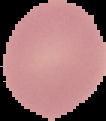

Summary:
  - Image size: 106×121 pixels
  - Image type: cell region segmented out of the field of view; surrounding area masked to black
  - Preparation: thin blood smear
  - Result: negative for malaria parasites